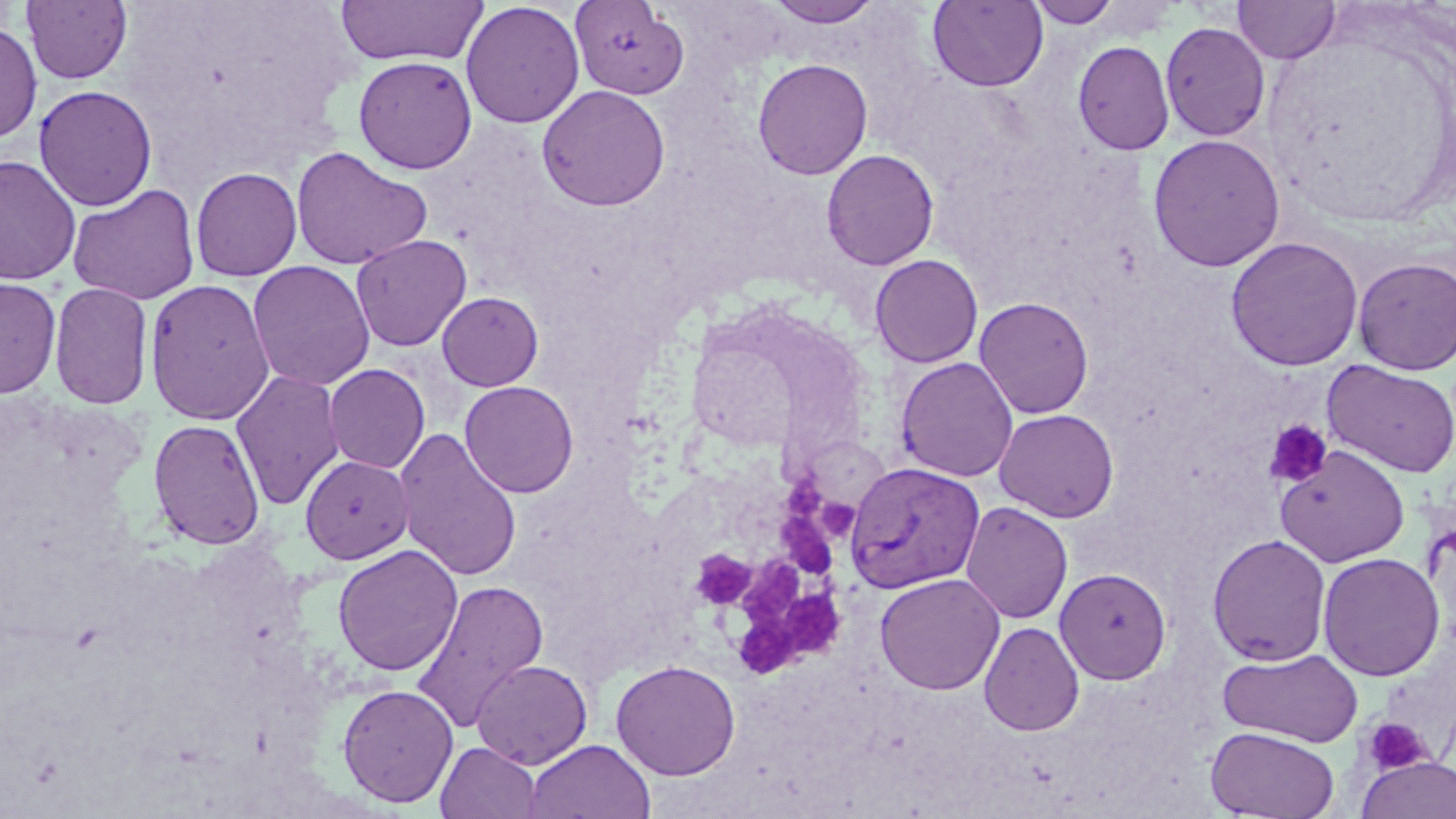
Approximate bounding boxes as (x1,y1)-(x2,y2) corner pairs in pixels. Plasmodium vivax-infected red blood cell locations: (843,461)-(985,594). Platelet locations: (1264,420)-(1332,488), (780,464)-(824,525), (814,493)-(857,542), (775,510)-(841,581), (694,553)-(760,605), (740,556)-(806,625), (787,586)-(843,660), (736,617)-(807,683), (1363,717)-(1432,775). Uninfected red blood cell locations: (766,0)-(882,27), (927,0)-(1049,92), (1027,0)-(1121,28), (1233,0)-(1340,64), (21,1)-(133,84), (335,1)-(489,66), (569,1)-(690,100), (460,2)-(585,128), (1160,21)-(1270,142), (0,23)-(42,144), (1073,40)-(1175,155), (353,56)-(477,174), (752,58)-(873,180), (34,84)-(158,211), (536,84)-(671,211), (1147,134)-(1286,272), (291,146)-(432,270), (821,149)-(939,270), (0,155)-(81,287), (190,167)-(303,282), (67,184)-(200,305), (350,234)-(472,351), (1225,236)-(1364,371), (869,254)-(983,368), (1352,257)-(1456,375), (247,260)-(375,391), (0,277)-(61,398), (144,278)-(275,426), (48,281)-(154,410), (436,291)-(543,391), (973,296)-(1094,419), (895,357)-(1019,482), (1321,360)-(1456,478), (324,364)-(430,473), (230,370)-(345,510), (459,380)-(580,498), (993,408)-(1120,522), (147,418)-(266,550), (393,427)-(523,582), (1275,445)-(1410,567), (300,454)-(414,564), (960,501)-(1073,624), (1207,534)-(1331,666), (332,544)-(463,676), (1317,552)-(1445,681), (1054,567)-(1171,684), (875,572)-(1006,695), (409,579)-(549,734), (979,621)-(1085,736), (1217,647)-(1364,748), (471,659)-(592,769), (610,660)-(741,780), (337,683)-(459,808), (1205,727)-(1340,818), (523,738)-(656,819), (436,741)-(541,819), (1358,756)-(1456,819). Slide-level diagnosis: Plasmodium vivax. Captured at 1000x magnification. May-Grünwald-Giemsa-stained preparation. Light microscopy. Image is 1456×819 pixels. Single field of view. Thin blood film.